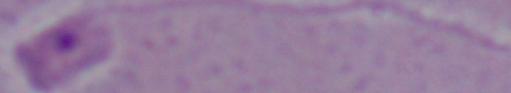

Summary:
  - Identification: Leishmania
  - Magnification: 1000x
  - Modality: micrograph